Assess the morphology of the red blood cells.
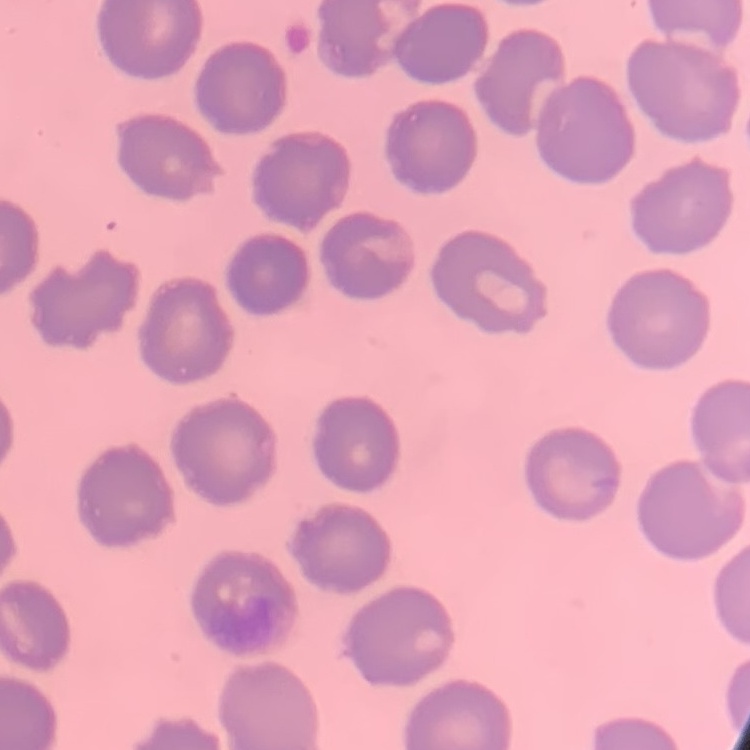
No rouleaux formation.

image type = square crop of a larger photomicrograph
preparation = thin blood smear
stain = Field's or Giemsa